Locate Plasmodium parasites and leukocytes.
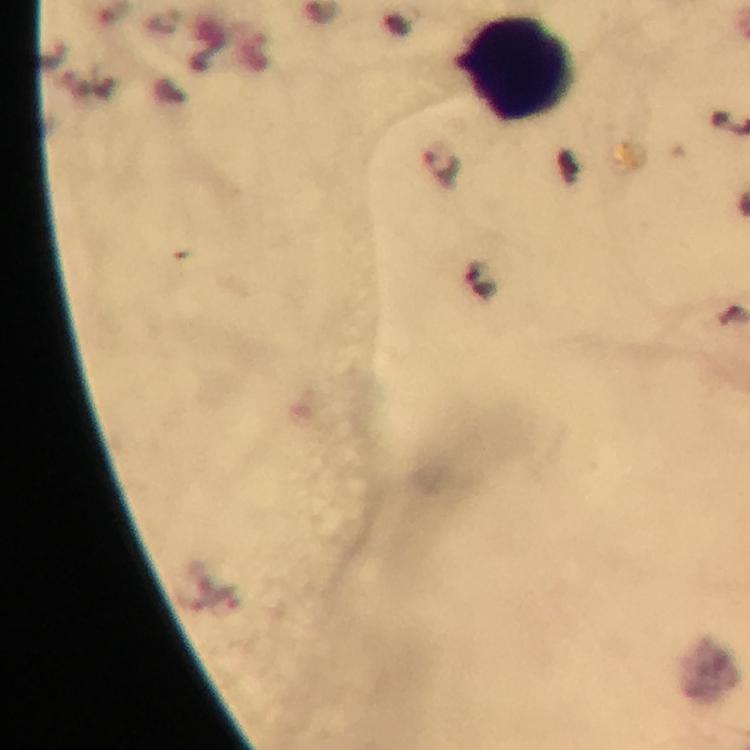

Approximate object centers, in pixels from the top-left corner.
Plasmodium parasites: (x=441, y=166).
Leukocytes: (x=515, y=67).

Summary:
  - Context: from a malaria diagnostic workup
  - Stain: Giemsa
  - Immersion oil: applied
  - Image size: 750×750 pixels
  - Preparation: thick blood smear
  - Magnification: 100x
  - Cropped from: one field of view
  - Capture: smartphone photograph through a microscope